Identify the cell.
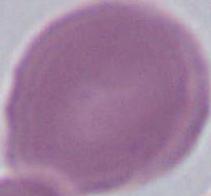

This is an erythrocyte.

Summary:
  - Modality: micrograph
  - Magnification: 1000x